Assess this cell for malaria.
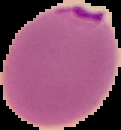
Parasitized.

Summary:
  - Image type: segmented cell region with the area outside set to black
  - Image size: 121×130 pixels
  - Preparation: thin blood film